Assess this cell for malaria.
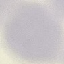
It is uninfected.

image type = automatically extracted cell patch, resized to 64 × 64 pixels
capture = smartphone camera at the microscope eyepiece
preparation = thin blood film
stain = Giemsa